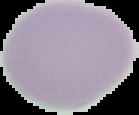
Summary:
  - Malaria status: uninfected
  - Image type: cell region segmented out of the field of view; surrounding area masked to black
  - Image size: 139×115 pixels
  - Preparation: thin blood film